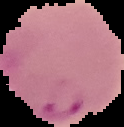

Summary:
  - Image size: 124×127 pixels
  - Preparation: thin blood smear
  - Malaria status: parasitized
  - Image type: cell region segmented out of the field of view; surrounding area masked to black